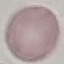

Summary:
  - Malaria status: uninfected
  - Capture: smartphone camera at the microscope eyepiece
  - Stain: Giemsa
  - Preparation: thin blood smear
  - Image type: cell patch, automatically extracted from a larger field of view and resized to 64 × 64 pixels